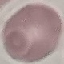
malaria status = uninfected
capture = smartphone camera at the microscope eyepiece
stain = Giemsa
image type = cell patch, automatically extracted from a larger field of view and resized to 64 × 64 pixels
preparation = thin smear